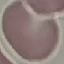
malaria status = uninfected
image type = automatically extracted cell patch, resized to 64 × 64 pixels
stain = Giemsa
preparation = thin blood film
capture = smartphone through the microscope eyepiece